Name the parasite shown.
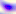
Toxoplasma gondii.

{
  "magnification": "400x",
  "modality": "micrograph"
}